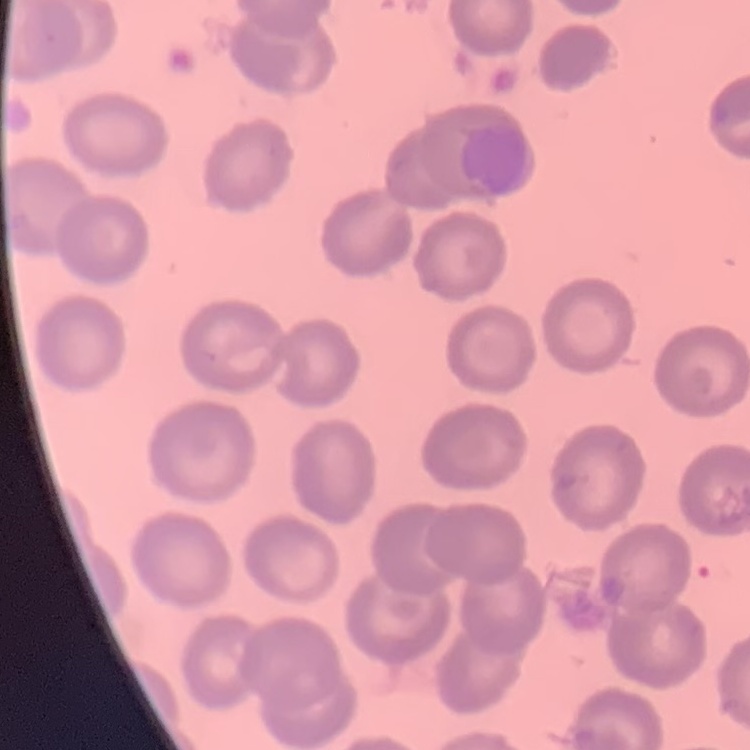
Summary:
  - Red blood cell morphology: no rouleaux formation
  - Stain: Field's or Giemsa
  - Image type: one tile cut from a larger photomicrograph
  - Preparation: thin peripheral smear